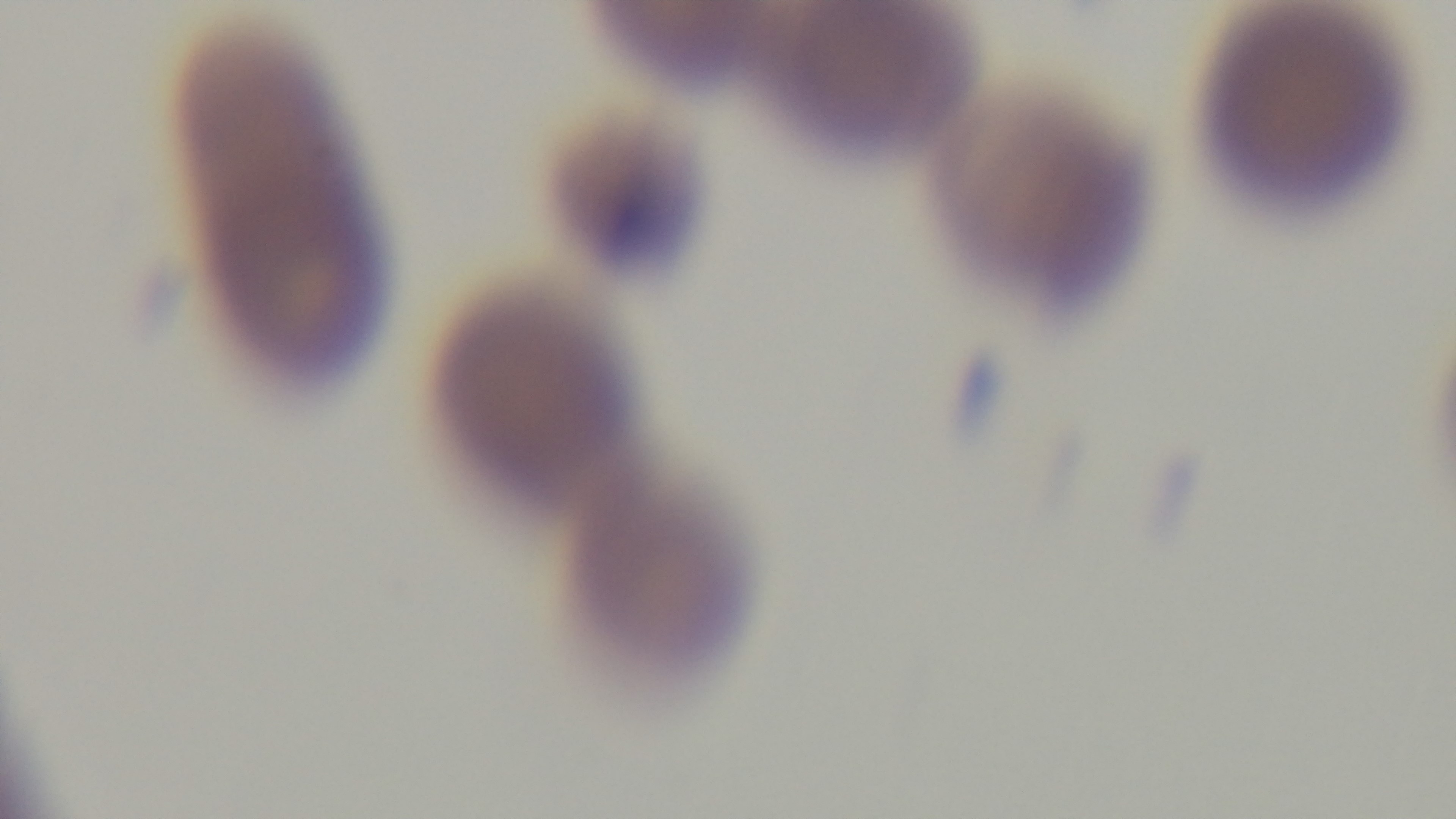

Light microscopy. Malaria status: infected. Giemsa-stained. Mounted 4K digital camera. 100x oil-immersion objective. Preparation: thin blood film. One field from the slide.